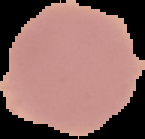

Summary:
  - Preparation: thin blood film
  - Image size: 145×139 pixels
  - Image type: cell region segmented out of the field of view; surrounding area masked to black
  - Result: no Plasmodium parasites detected